Report the malaria status of this cell.
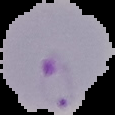

It is parasitized.

Summary:
  - Image type: segmented cell region on a black background
  - Preparation: thin blood smear
  - Image size: 115×115 pixels